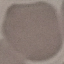
result = no malaria parasites detected
stain = Giemsa
capture = smartphone through the microscope eyepiece
image type = cell patch, automatically extracted from a larger field of view and resized to 64 × 64 pixels
preparation = thin smear